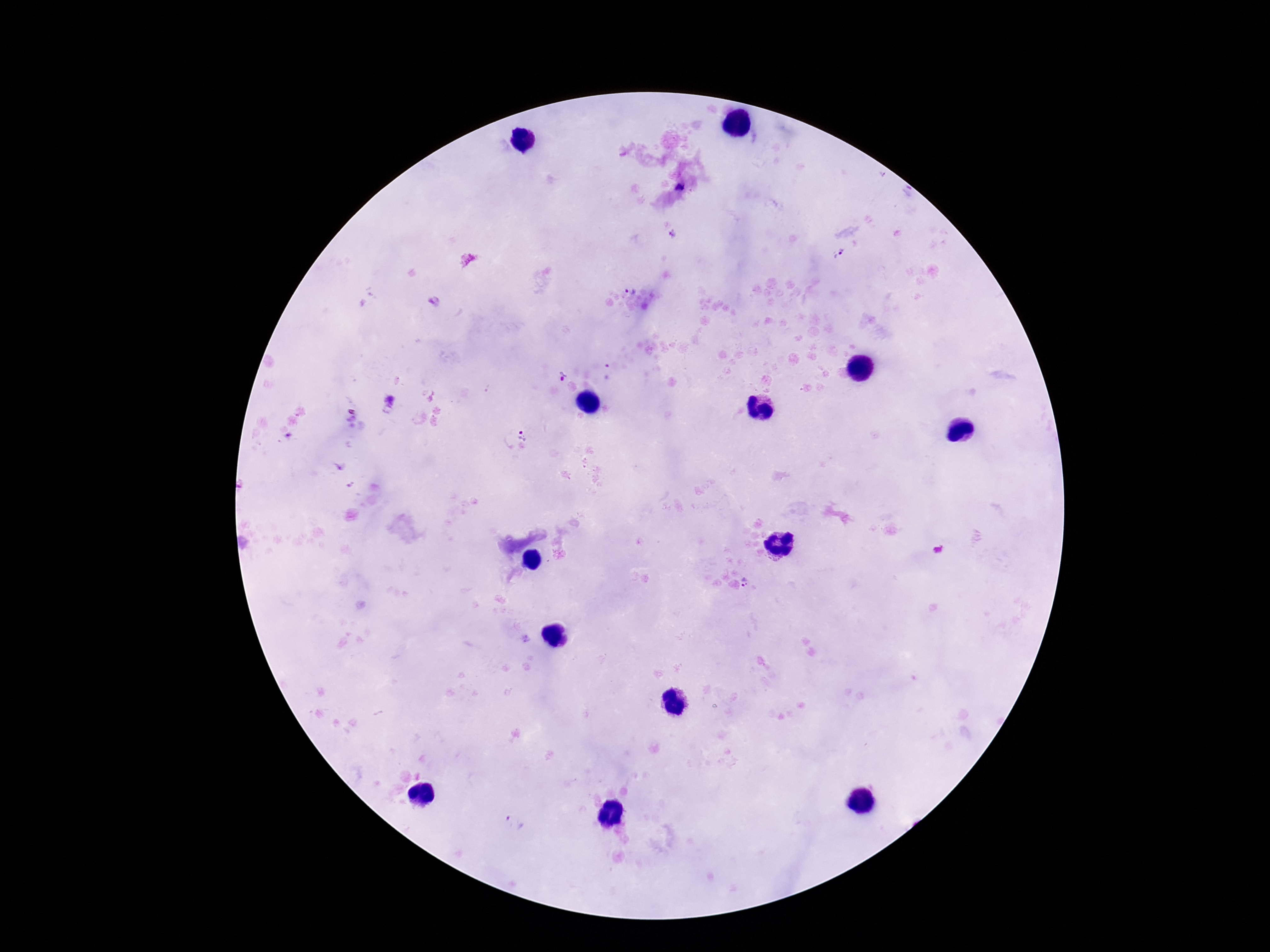

Approximate centers as {x, y} in pixels.
Summary:
  - Plasmodium parasite locations: {680, 188}, {674, 235}, {838, 253}, {629, 287}, {606, 371}, {561, 376}, {523, 433}, {748, 583}, {527, 639}, {514, 823}
  - Capture: smartphone camera through the microscope eyepiece
  - Image size: 1270×952 pixels
  - Preparation: thick blood smear
  - Patient malaria status: infected
  - Magnification: 100x
  - Stain: Giemsa
  - Field of view: single